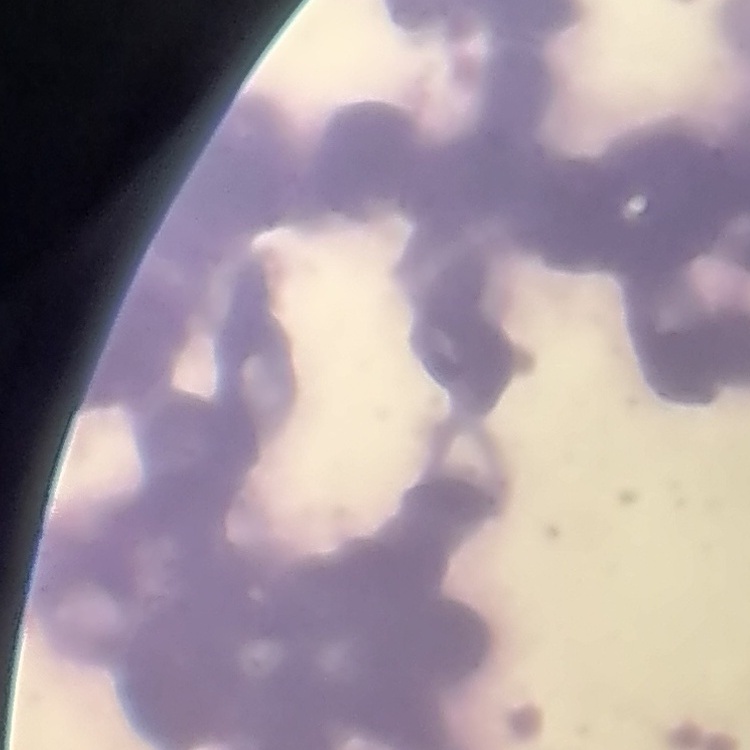
Summary:
  - Red blood cell morphology: rouleaux formation
  - Stain: Field's or Giemsa
  - Image type: square crop of a larger photomicrograph
  - Preparation: thin blood film